Assess this cell for malaria.
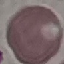

It is uninfected.

capture: smartphone through the microscope eyepiece
image_type: cell patch, automatically extracted from a larger field of view and resized to 64 × 64 pixels
stain: Giemsa
preparation: thin blood film